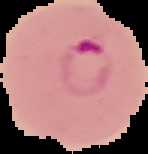
Malaria status: parasitized. Image is 148×154 pixels. From a thin blood smear. The area outside the segmented cell region is set to black.